Name the parasite shown.
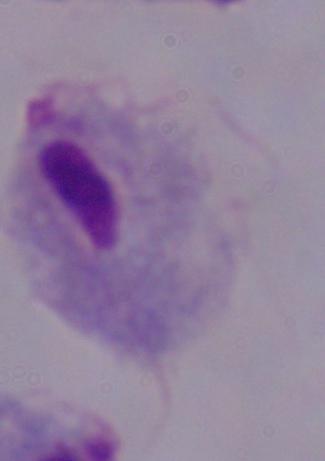

A trichomonad.

Summary:
  - Magnification: 1000x
  - Modality: micrograph